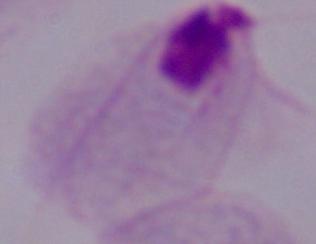
Summary:
  - Modality: photomicrograph
  - Identification: trichomonad
  - Magnification: 1000x